Assess this cell for malaria.
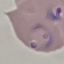
Parasitized.

image type = cell patch, automatically extracted from a larger field of view and resized to 64 × 64 pixels
preparation = thin blood smear
capture = smartphone through the microscope eyepiece
stain = Giemsa